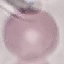
malaria_status: uninfected
image_type: cell patch, automatically extracted from a larger field of view and resized to 64 × 64 pixels
stain: Giemsa
preparation: thin smear
capture: smartphone through the microscope eyepiece